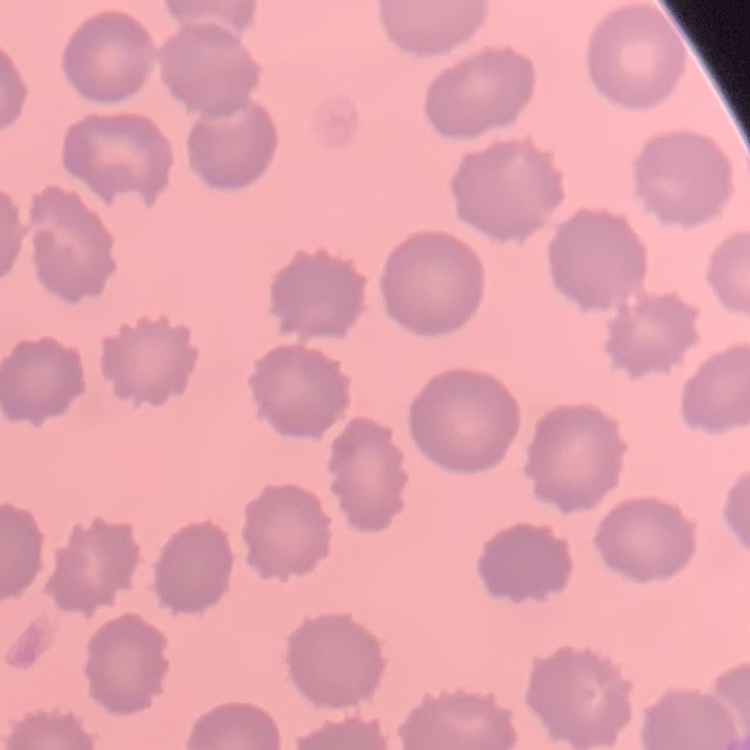
The red blood cells exhibit no rouleaux formation. One tile cut from a larger photomicrograph. Thin blood film. Field's or Giemsa stain.